Assess this cell for malaria.
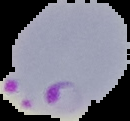

Parasitized.

image size = 130×121 pixels
preparation = thin blood smear
image type = cell region segmented out of the field of view; surrounding area masked to black